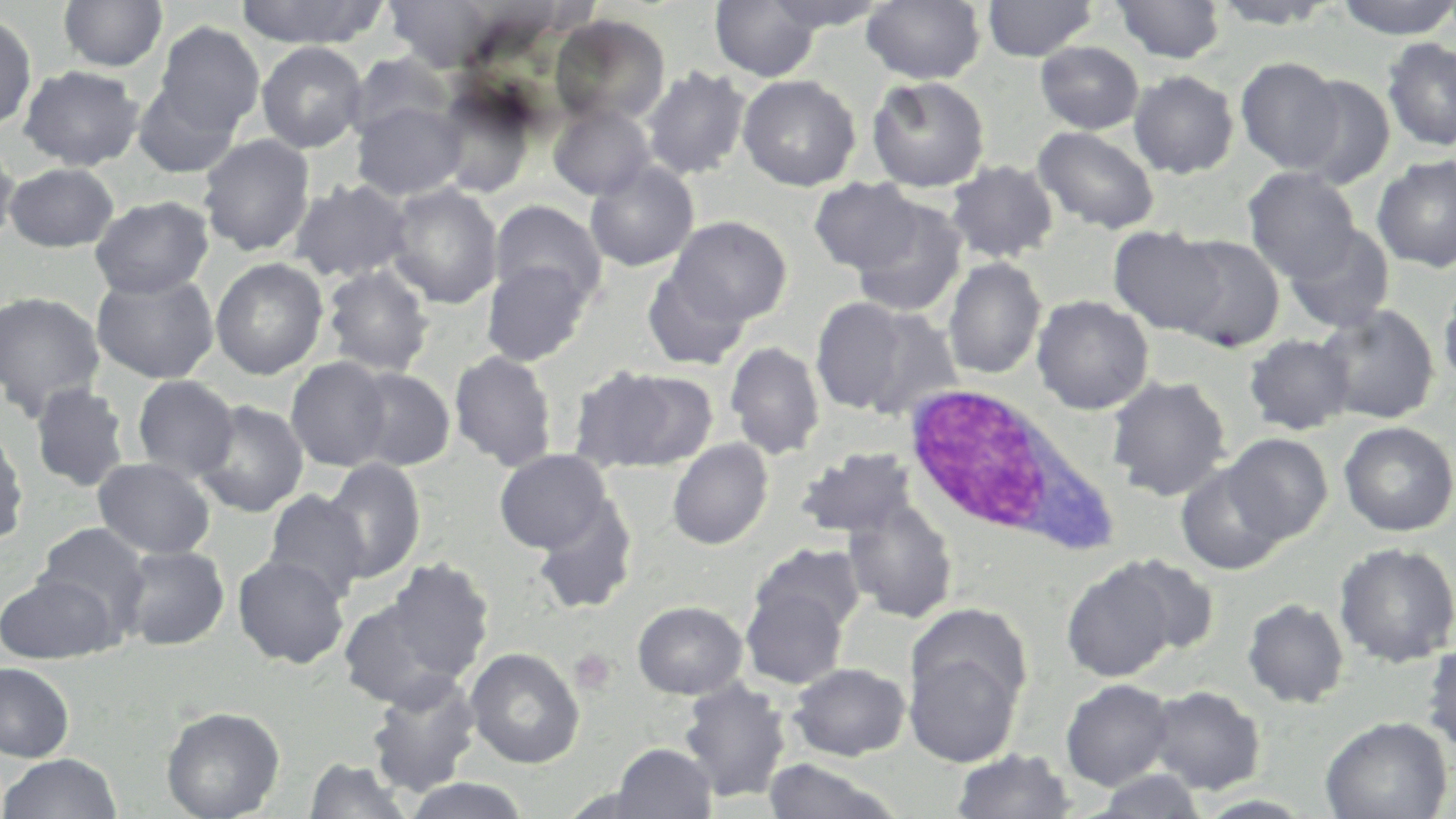
Summary:
  - Coordinate format: approximate bounding boxes as named x1/y1/x2/y2 corners in pixels
  - Uninfected red blood cell locations: (x1=57, y1=0, x2=169, y2=73), (x1=234, y1=0, x2=389, y2=48), (x1=383, y1=0, x2=498, y2=73), (x1=710, y1=0, x2=822, y2=82), (x1=763, y1=0, x2=890, y2=32), (x1=861, y1=0, x2=985, y2=85), (x1=982, y1=0, x2=1099, y2=61), (x1=1111, y1=0, x2=1226, y2=64), (x1=1209, y1=0, x2=1342, y2=29), (x1=1335, y1=0, x2=1456, y2=40), (x1=0, y1=9, x2=38, y2=134), (x1=550, y1=14, x2=671, y2=125), (x1=154, y1=21, x2=265, y2=136), (x1=1381, y1=37, x2=1456, y2=152), (x1=256, y1=41, x2=368, y2=153), (x1=1035, y1=41, x2=1144, y2=134), (x1=347, y1=52, x2=455, y2=142), (x1=1235, y1=57, x2=1345, y2=173), (x1=18, y1=65, x2=144, y2=170), (x1=641, y1=66, x2=751, y2=180), (x1=1128, y1=70, x2=1240, y2=178), (x1=738, y1=74, x2=861, y2=191), (x1=866, y1=75, x2=991, y2=192), (x1=1291, y1=75, x2=1396, y2=189), (x1=133, y1=78, x2=244, y2=179), (x1=432, y1=84, x2=537, y2=196), (x1=352, y1=101, x2=467, y2=201), (x1=548, y1=103, x2=655, y2=200), (x1=1033, y1=125, x2=1160, y2=235), (x1=198, y1=134, x2=316, y2=257), (x1=0, y1=137, x2=19, y2=250), (x1=1372, y1=154, x2=1456, y2=273), (x1=584, y1=160, x2=699, y2=272), (x1=945, y1=160, x2=1059, y2=264), (x1=4, y1=163, x2=119, y2=252), (x1=1242, y1=167, x2=1362, y2=281), (x1=289, y1=178, x2=414, y2=283), (x1=809, y1=178, x2=925, y2=275), (x1=385, y1=183, x2=504, y2=309), (x1=90, y1=195, x2=214, y2=299), (x1=848, y1=198, x2=969, y2=319), (x1=489, y1=201, x2=606, y2=309), (x1=667, y1=216, x2=792, y2=325), (x1=1283, y1=223, x2=1396, y2=334), (x1=1108, y1=226, x2=1227, y2=335), (x1=1166, y1=234, x2=1286, y2=352), (x1=210, y1=257, x2=328, y2=380), (x1=942, y1=257, x2=1046, y2=380), (x1=480, y1=258, x2=593, y2=367), (x1=321, y1=263, x2=436, y2=378), (x1=641, y1=265, x2=754, y2=371), (x1=91, y1=271, x2=219, y2=384), (x1=1438, y1=277, x2=1456, y2=390), (x1=0, y1=291, x2=106, y2=419), (x1=1031, y1=295, x2=1154, y2=415), (x1=811, y1=297, x2=922, y2=416), (x1=1315, y1=303, x2=1440, y2=425), (x1=845, y1=305, x2=967, y2=422), (x1=1244, y1=334, x2=1355, y2=435), (x1=725, y1=341, x2=825, y2=460), (x1=449, y1=350, x2=558, y2=472), (x1=285, y1=357, x2=393, y2=472), (x1=570, y1=364, x2=713, y2=471), (x1=349, y1=367, x2=456, y2=471), (x1=131, y1=374, x2=240, y2=483), (x1=1106, y1=375, x2=1232, y2=501), (x1=30, y1=381, x2=132, y2=493), (x1=193, y1=399, x2=310, y2=517), (x1=0, y1=419, x2=30, y2=551), (x1=1338, y1=421, x2=1456, y2=536), (x1=1222, y1=433, x2=1332, y2=544), (x1=667, y1=438, x2=773, y2=550), (x1=795, y1=447, x2=920, y2=541), (x1=493, y1=449, x2=613, y2=554), (x1=92, y1=457, x2=216, y2=559), (x1=322, y1=458, x2=425, y2=584), (x1=1176, y1=462, x2=1288, y2=575), (x1=263, y1=490, x2=371, y2=603), (x1=532, y1=496, x2=639, y2=616), (x1=842, y1=496, x2=959, y2=624), (x1=34, y1=522, x2=152, y2=635), (x1=1333, y1=541, x2=1456, y2=668), (x1=751, y1=543, x2=866, y2=635), (x1=118, y1=545, x2=230, y2=651), (x1=232, y1=553, x2=350, y2=669), (x1=1112, y1=554, x2=1221, y2=658), (x1=381, y1=558, x2=494, y2=682), (x1=1061, y1=560, x2=1180, y2=682), (x1=0, y1=573, x2=119, y2=664), (x1=740, y1=585, x2=848, y2=689), (x1=338, y1=597, x2=466, y2=710), (x1=1242, y1=598, x2=1350, y2=709), (x1=632, y1=601, x2=748, y2=699), (x1=1422, y1=638, x2=1456, y2=757), (x1=903, y1=641, x2=1025, y2=768), (x1=465, y1=647, x2=585, y2=769), (x1=0, y1=662, x2=75, y2=762), (x1=788, y1=662, x2=911, y2=761), (x1=365, y1=672, x2=482, y2=797), (x1=1060, y1=678, x2=1175, y2=790), (x1=678, y1=679, x2=791, y2=804), (x1=1146, y1=685, x2=1266, y2=795), (x1=161, y1=705, x2=285, y2=819), (x1=1320, y1=715, x2=1452, y2=819), (x1=611, y1=743, x2=716, y2=819), (x1=950, y1=748, x2=1077, y2=818), (x1=0, y1=752, x2=124, y2=819), (x1=304, y1=758, x2=414, y2=818), (x1=762, y1=758, x2=900, y2=818), (x1=1089, y1=770, x2=1209, y2=818), (x1=400, y1=777, x2=532, y2=818)
  - White blood cell locations: (x1=900, y1=384, x2=1106, y2=549)
  - Platelet locations: (x1=569, y1=648, x2=617, y2=695)
  - Slide-level diagnosis: no evidence of blood parasites
  - Field of view: single
  - Image size: 1456×819 pixels
  - Preparation: thin blood film
  - Magnification: 1000x
  - Stain: May-Grünwald-Giemsa
  - Modality: optical microscopy